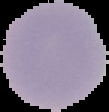

Summary:
  - Image type: segmented cell region on a black background
  - Image size: 109×112 pixels
  - Preparation: thin blood film
  - Malaria status: uninfected